Identify the parasite.
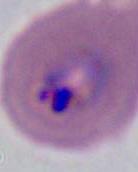
This is Plasmodium.

Micrograph. 400x or 1000x magnification.